Locate and identify every blood parasite.
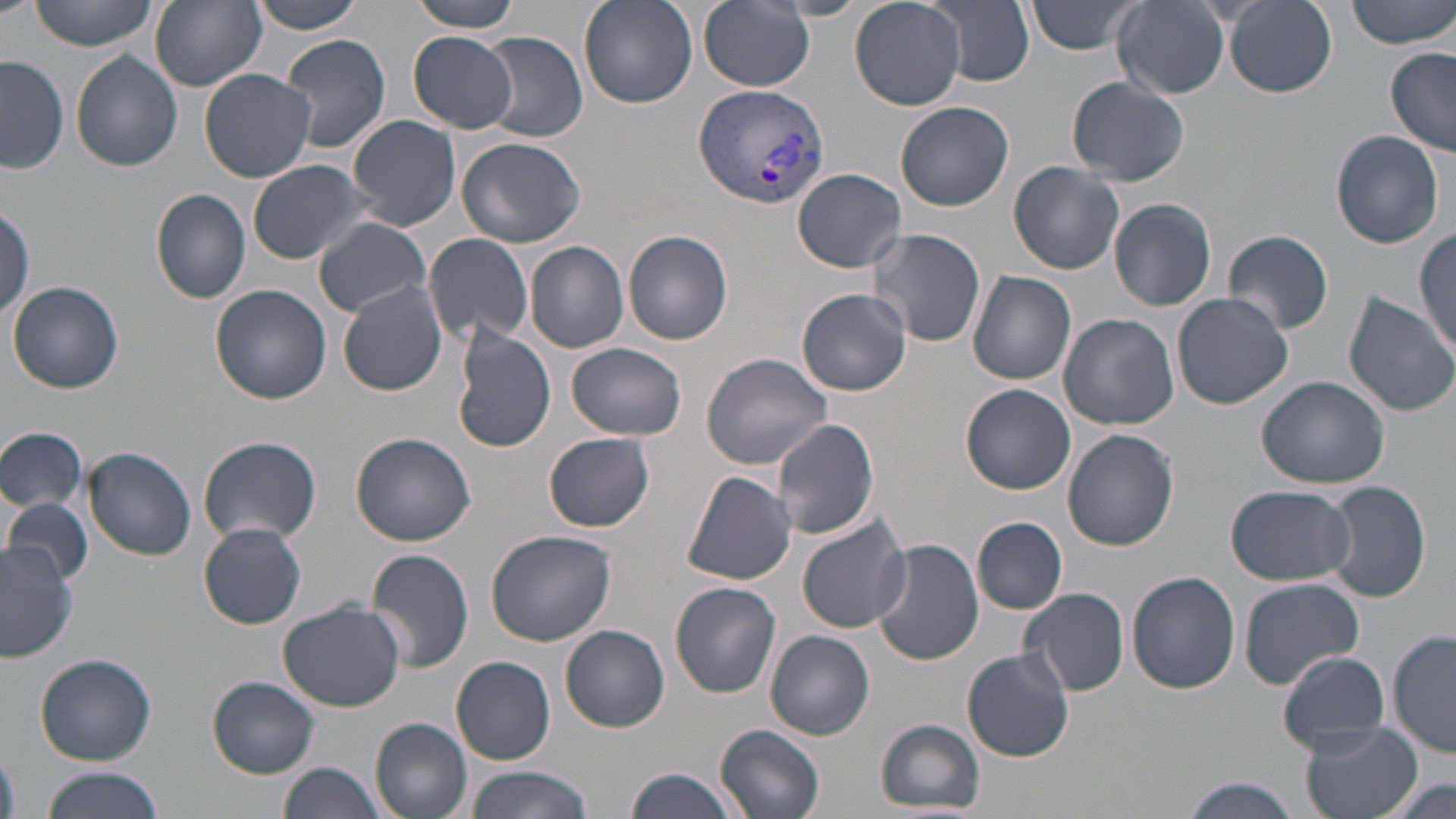
Approximate bounding boxes as (x1,y1)-(x2,y2) corner pairs in pixels.
Plasmodium vivax-infected red blood cells: (693,82)-(829,211).
No Plasmodium falciparum, Plasmodium ovale, Plasmodium malariae, Babesia divergens, or Trypanosoma brucei observed.

Summary:
  - Uninfected red blood cell locations: (27,0)-(159,51), (247,0)-(371,33), (408,0)-(522,31), (579,0)-(698,108), (700,0)-(813,91), (850,0)-(966,111), (923,0)-(1036,88), (1028,0)-(1142,55), (1225,0)-(1336,96), (1348,0)-(1456,50), (150,1)-(267,91), (1113,2)-(1229,100), (407,31)-(517,134), (476,32)-(588,142), (279,33)-(392,153), (1386,48)-(1456,158), (70,49)-(184,172), (1,54)-(70,174), (198,68)-(318,182), (1067,76)-(1189,187), (896,102)-(1015,212), (347,115)-(462,231), (1329,131)-(1444,249), (455,136)-(585,248), (247,158)-(381,265), (1009,159)-(1125,274), (793,167)-(907,272), (152,189)-(251,303), (1108,198)-(1218,312), (0,200)-(33,324), (312,216)-(432,317), (1414,225)-(1456,355), (867,228)-(987,348), (1223,228)-(1334,335), (624,230)-(732,345), (424,233)-(534,346), (525,241)-(628,354), (968,271)-(1077,385), (338,279)-(448,396), (995,279)-(1162,407), (8,281)-(125,394), (209,284)-(331,403), (797,288)-(912,396), (1343,292)-(1456,416), (1172,293)-(1293,409), (1058,313)-(1178,430), (451,326)-(555,454), (567,342)-(689,439), (556,345)-(675,529), (700,352)-(835,469), (1258,377)-(1390,488), (960,384)-(1076,495), (769,418)-(880,540), (0,425)-(88,515), (1062,429)-(1178,551), (349,432)-(476,546), (544,433)-(656,532), (198,435)-(322,545), (84,446)-(196,562), (682,470)-(798,585), (1322,480)-(1432,604), (1226,484)-(1354,587), (2,494)-(93,589), (797,515)-(910,633), (971,517)-(1068,614), (199,522)-(307,629), (485,530)-(617,646), (0,537)-(79,667), (871,538)-(982,666), (366,548)-(474,674), (1127,571)-(1240,694), (1239,576)-(1367,688), (670,581)-(781,698), (1020,586)-(1129,696), (277,600)-(405,712), (561,624)-(670,731), (766,630)-(874,740), (1389,630)-(1455,759), (961,647)-(1076,763), (1276,651)-(1393,755), (36,653)-(157,765), (451,656)-(556,764), (209,677)-(319,777), (371,718)-(474,819), (875,718)-(986,815), (1298,720)-(1424,819), (714,725)-(825,819), (279,761)-(389,819), (463,765)-(590,819), (622,767)-(742,819), (37,768)-(164,819), (1178,777)-(1304,818), (1380,777)-(1456,819)
  - Slide-level diagnosis: Plasmodium vivax
  - Magnification: 1000x
  - Image size: 1456×819 pixels
  - Stain: May-Grünwald-Giemsa
  - Preparation: thin blood film
  - Modality: optical microscopy
  - Field of view: single